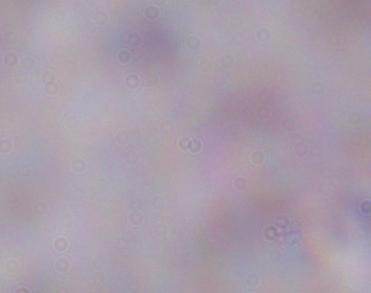
Photomicrograph. A trypanosome is shown. Captured at 1000x magnification.